Classify this cell by malaria status.
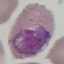
It is uninfected.

Acquired by smartphone through the microscope eyepiece. Giemsa-stained preparation. Cell patch, automatically extracted from a larger field of view and resized to 64 × 64 pixels. Thin blood film.